Locate every Plasmodium parasite and every leukocyte.
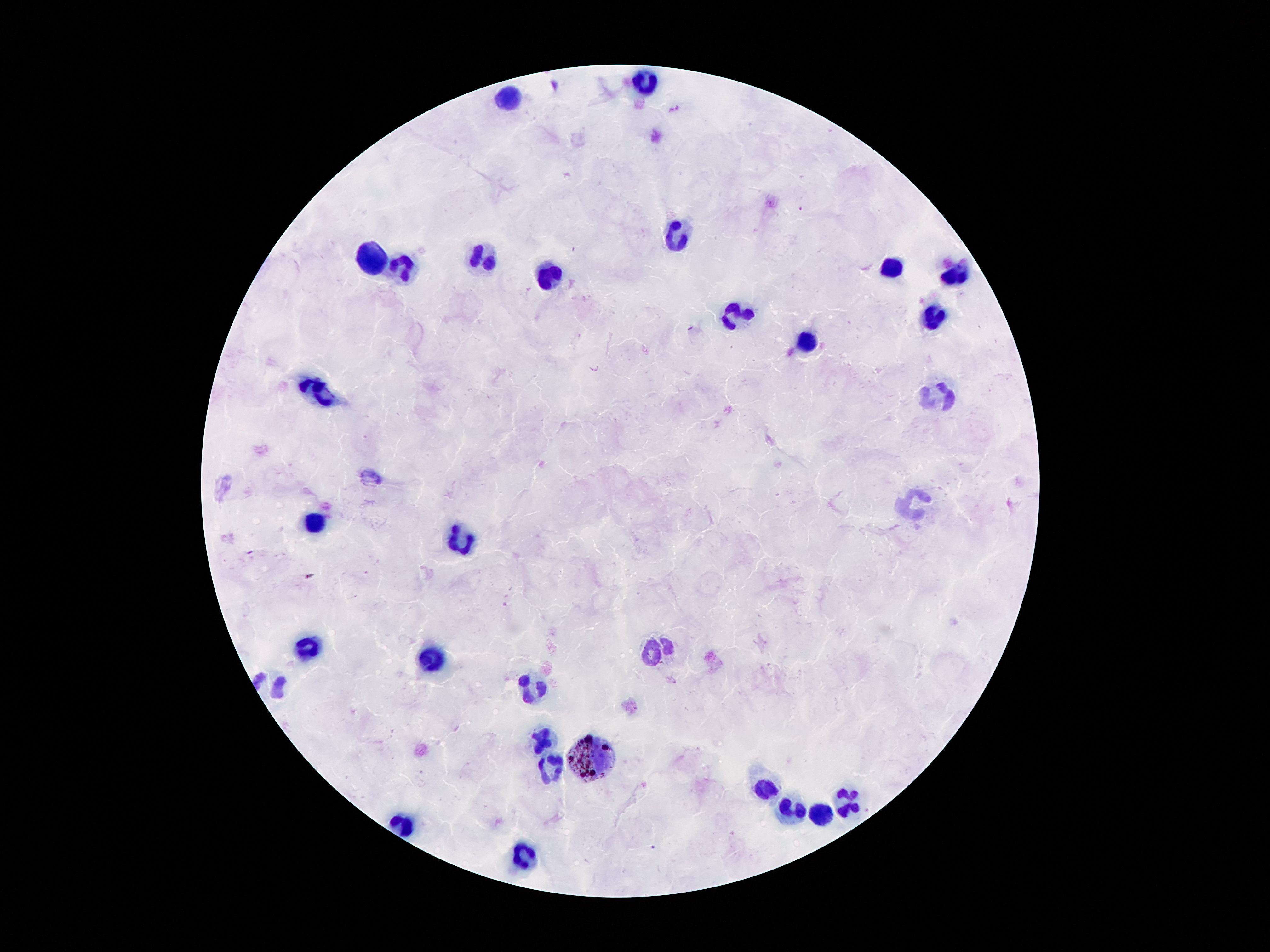

Approximate centers as {x, y} in pixels.
Plasmodium parasites: {801, 208}, {250, 552}, {310, 575}, {654, 848}.
Leukocytes: {647, 82}, {511, 99}, {675, 234}, {375, 257}, {486, 257}, {887, 265}, {402, 270}, {551, 275}, {954, 275}, {736, 312}, {931, 316}, {807, 343}, {320, 388}, {941, 396}, {916, 503}, {312, 522}, {463, 543}, {309, 648}, {652, 652}, {433, 658}, {532, 687}, {545, 738}, {587, 758}, {547, 767}, {765, 786}, {847, 802}, {796, 810}, {817, 814}, {402, 826}, {526, 859}.

Summary:
  - Patient malaria status: infected with Plasmodium falciparum
  - Stain: Giemsa
  - Preparation: thick blood smear
  - Image size: 1270×952 pixels
  - Magnification: 100x
  - Capture: smartphone through the microscope eyepiece
  - Field of view: single